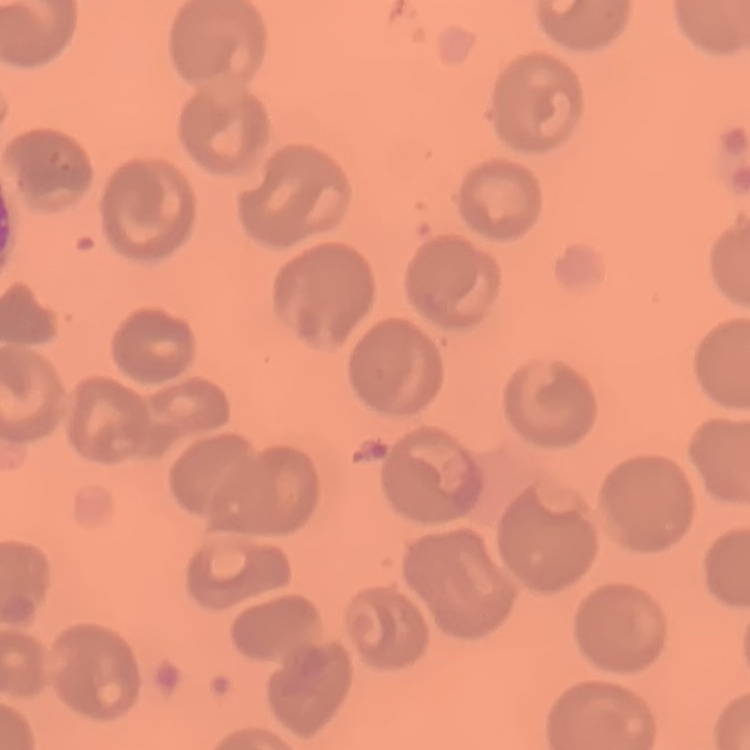

Summary:
  - Red blood cell morphology: no rouleaux formation
  - Stain: Field's or Giemsa
  - Preparation: thin peripheral smear
  - Image type: one tile cut from a larger photomicrograph